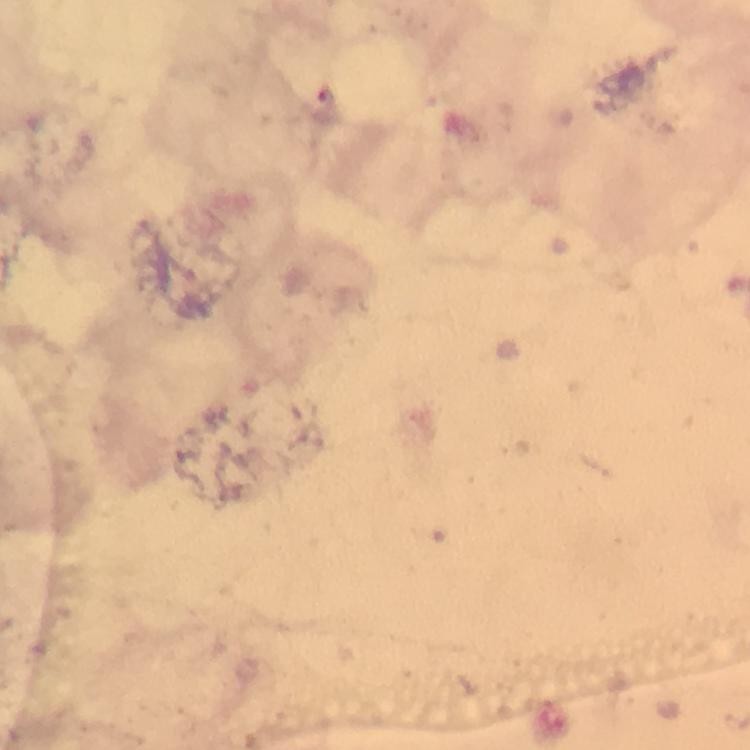

Approximate object centers, in pixels from the top-left corner.
Summary:
  - Plasmodium parasite locations: (x=330, y=97)
  - Preparation: thick blood film
  - Context: from a malaria diagnostic workup
  - Capture: smartphone mounted on the microscope
  - Cropped from: one field of view
  - Stain: Giemsa
  - Immersion oil: used
  - Magnification: 100x
  - Image size: 750×750 pixels